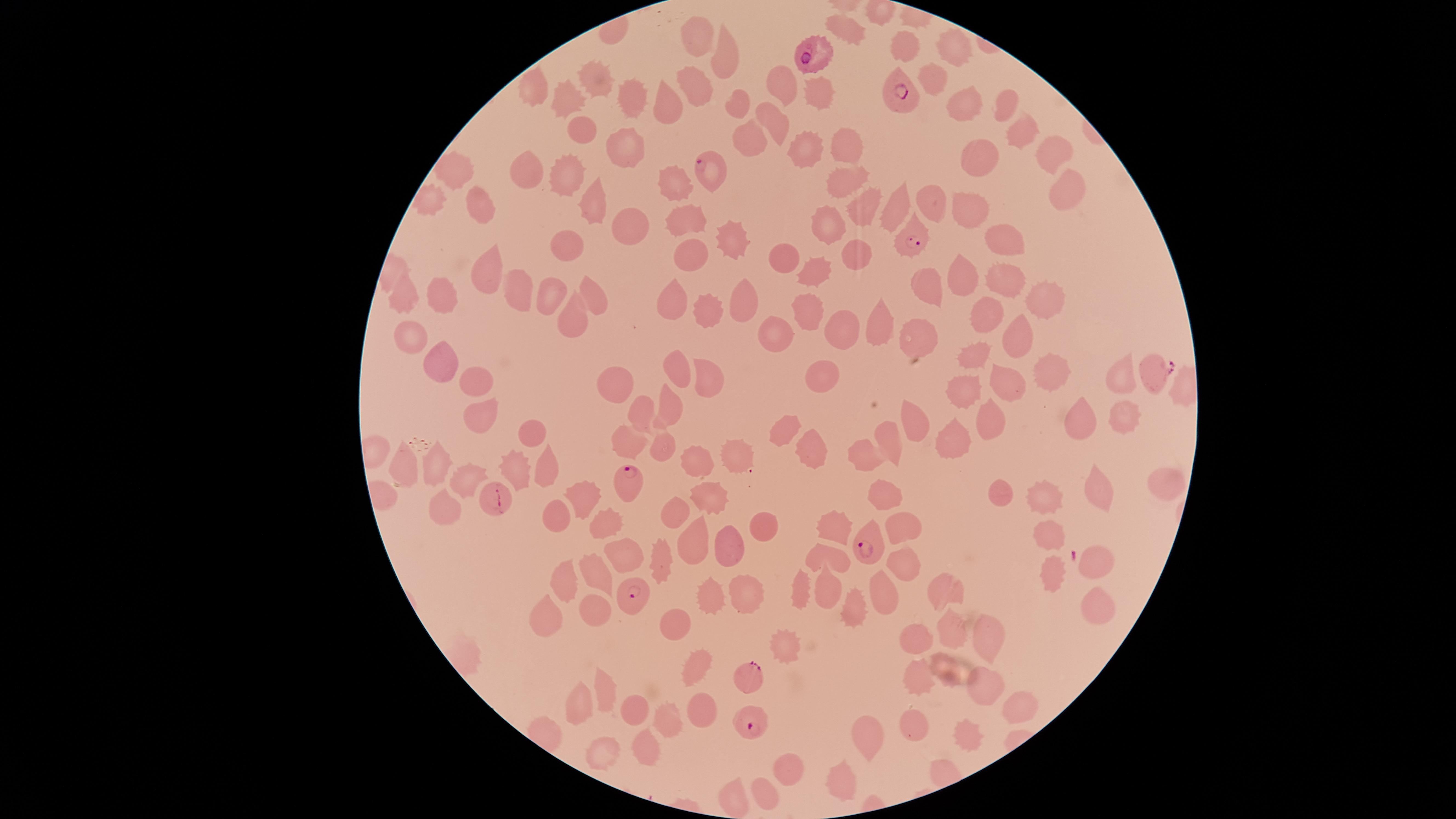 Approximate marker points as {x, y} in pixels. Uninfected red blood cells: {847, 27}, {705, 36}, {898, 48}, {951, 49}, {724, 59}, {594, 79}, {933, 80}, {696, 82}, {782, 82}, {818, 88}, {633, 90}, {534, 91}, {666, 96}, {569, 99}, {738, 101}, {1001, 107}, {962, 108}, {776, 120}, {1018, 130}, {580, 133}, {749, 141}, {839, 142}, {813, 147}, {1047, 148}, {629, 151}, {978, 162}, {524, 169}, {462, 172}, {841, 179}, {565, 180}, {1057, 182}, {675, 183}, {431, 196}, {929, 203}, {590, 204}, {894, 206}, {479, 207}, {965, 208}, {858, 211}, {825, 222}, {682, 228}, {622, 229}, {1003, 241}, {724, 242}, {565, 249}, {858, 252}, {693, 256}, {783, 258}, {823, 267}, {488, 269}, {960, 275}, {1007, 276}, {520, 288}, {924, 288}, {593, 290}, {402, 291}, {448, 296}, {1042, 296}, {679, 298}, {546, 301}, {742, 305}, {710, 308}, {812, 311}, {570, 314}, {882, 317}, {988, 320}, {911, 327}, {1015, 331}, {843, 333}, {774, 334}, {408, 338}, {976, 359}, {441, 362}, {703, 367}, {674, 368}, {1051, 369}, {1116, 373}, {826, 374}, {1005, 378}, {476, 382}, {618, 383}, {966, 388}, {669, 405}, {476, 411}, {992, 412}, {1126, 412}, {634, 413}, {1078, 415}, {912, 420}, {785, 424}, {535, 430}, {629, 439}, {954, 440}, {889, 441}, {812, 442}, {659, 446}, {722, 455}, {688, 456}, {863, 456}, {440, 468}, {406, 469}, {516, 470}, {545, 472}, {465, 477}, {1091, 486}, {1158, 488}, {1002, 490}, {1046, 494}, {880, 496}, {707, 497}, {587, 499}, {441, 503}, {674, 512}, {552, 515}, {845, 521}, {601, 522}, {762, 524}, {900, 526}, {1047, 536}, {691, 537}, {729, 551}, {620, 554}, {830, 559}, {1094, 563}, {660, 564}, {898, 564}, {1052, 568}, {593, 569}, {562, 581}, {800, 589}, {824, 590}, {947, 590}, {881, 591}, {749, 599}, {710, 602}, {858, 604}, {1094, 607}, {590, 609}, {542, 614}, {951, 625}, {676, 628}, {917, 636}, {994, 636}, {786, 645}, {694, 664}, {918, 673}, {984, 681}, {603, 697}, {633, 708}, {698, 708}, {1025, 708}, {575, 709}, {668, 720}, {911, 725}, {865, 730}, {962, 730}, {645, 746}, {605, 752}, {786, 766}, {842, 773}, {734, 792}, {761, 792}. Parasitized red blood cells: {813, 56}, {897, 95}, {715, 171}, {912, 243}, {1152, 372}, {628, 485}, {496, 498}, {870, 547}, {630, 593}, {753, 675}, {751, 722}. Presence: malaria parasites identified. Image is 1456×819 pixels. Giemsa stain. Circular visible region. Species: Plasmodium falciparum. Thin blood film. One field of view of the specimen. Smartphone photograph through the microscope eyepiece.